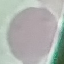
Malaria status: uninfected. Giemsa-stained preparation. Cell patch, automatically extracted from a larger field of view and resized to 64 × 64 pixels. Photographed with a smartphone camera at the microscope eyepiece. Thin smear of blood.